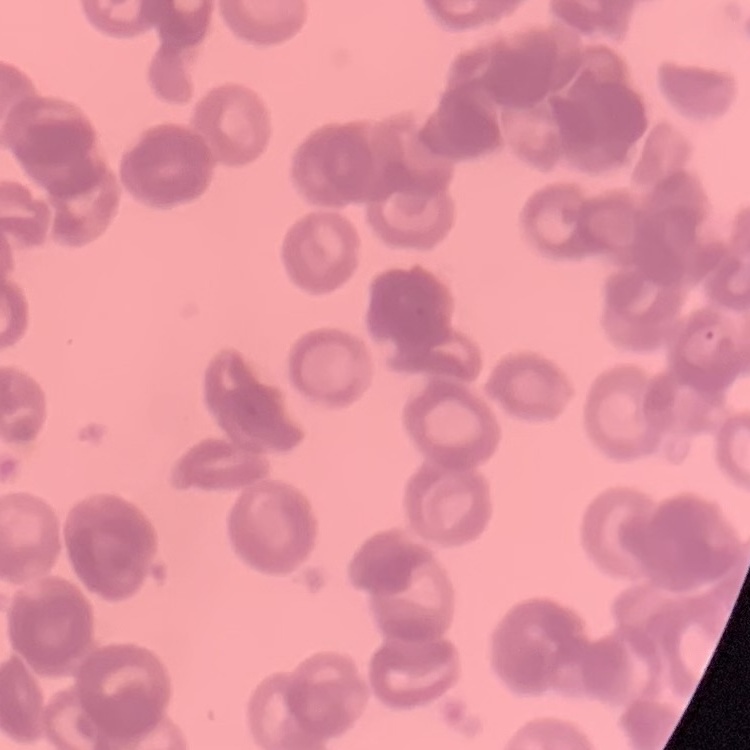

Summary:
  - Erythrocyte morphology: rouleaux formation
  - Stain: Field's or Giemsa
  - Image type: one tile cut from a larger photomicrograph
  - Preparation: thin peripheral smear